Locate platelets.
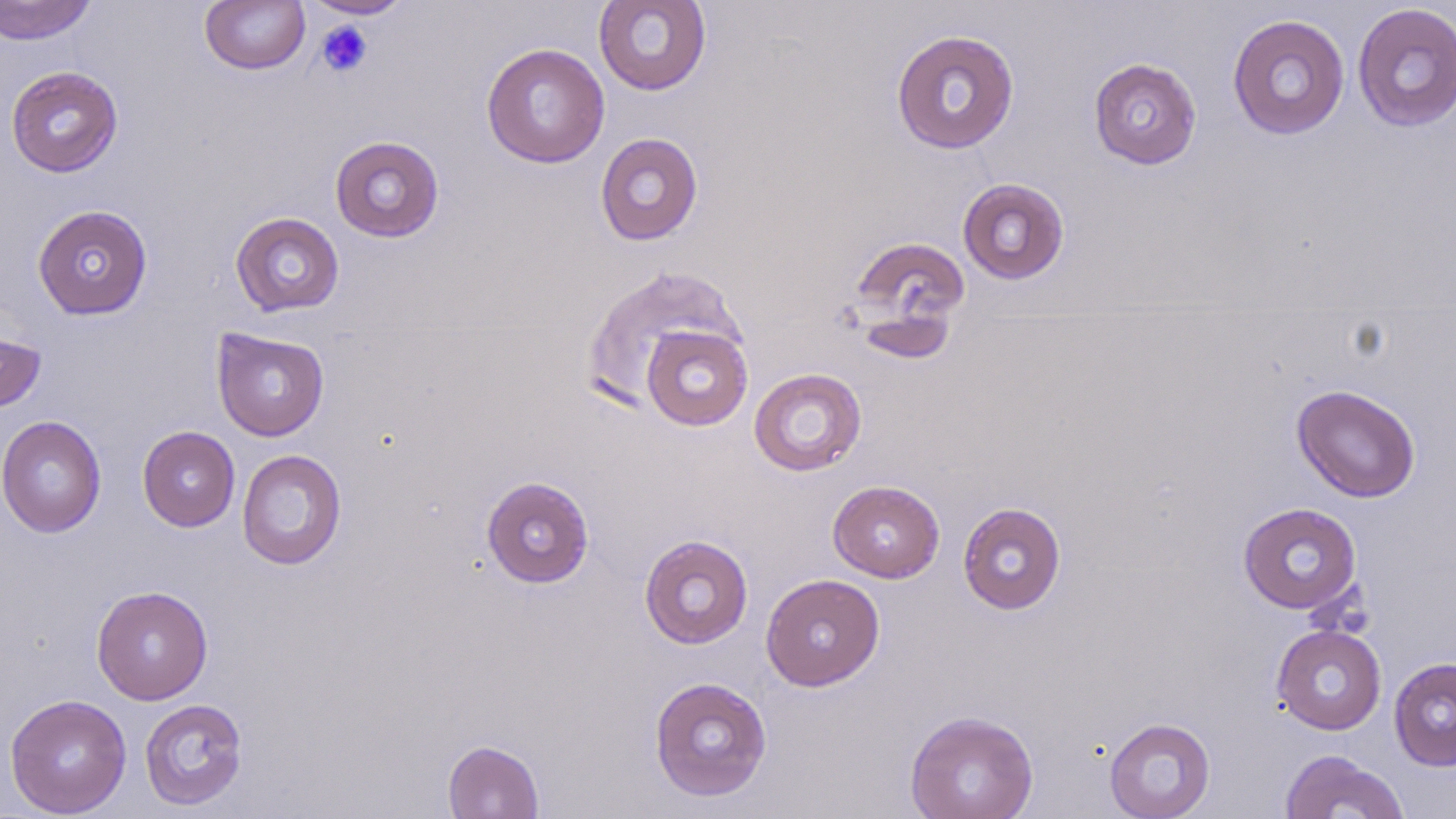
Approximate bounding boxes as (x1, y1, x2, y2) in pixels.
Platelets: (316, 20, 374, 78).

slide-level diagnosis = negative for blood parasites
stain = May-Grünwald-Giemsa
image size = 1456×819 pixels
preparation = thin blood film
modality = optical microscopy
field of view = one of a larger specimen
magnification = 1000x
uninfected red blood cell locations = approximate bounding boxes as (x1, y1, x2, y2) in pixels: (0, 0, 98, 44), (303, 0, 413, 19), (593, 0, 711, 96), (199, 1, 310, 74), (1351, 3, 1456, 132), (1227, 13, 1350, 140), (891, 29, 1020, 154), (481, 43, 610, 168), (1088, 57, 1202, 170), (5, 66, 123, 177), (595, 132, 704, 246), (329, 135, 444, 243), (957, 177, 1070, 285), (32, 204, 153, 320), (230, 212, 344, 317), (849, 236, 970, 331), (581, 265, 750, 415), (0, 323, 47, 414), (641, 324, 752, 431), (212, 327, 329, 441), (748, 367, 867, 477), (1291, 383, 1421, 503), (1, 415, 106, 538), (137, 426, 240, 532), (237, 449, 347, 570), (481, 475, 595, 588), (828, 480, 945, 583), (957, 501, 1067, 615), (1238, 502, 1362, 614), (639, 533, 753, 649), (760, 573, 885, 691), (91, 585, 213, 705), (1271, 624, 1387, 735), (1388, 656, 1456, 771), (648, 675, 772, 802), (4, 693, 132, 818), (139, 697, 249, 811), (904, 709, 1039, 819), (1104, 717, 1216, 818), (442, 739, 544, 818), (1279, 749, 1409, 819)